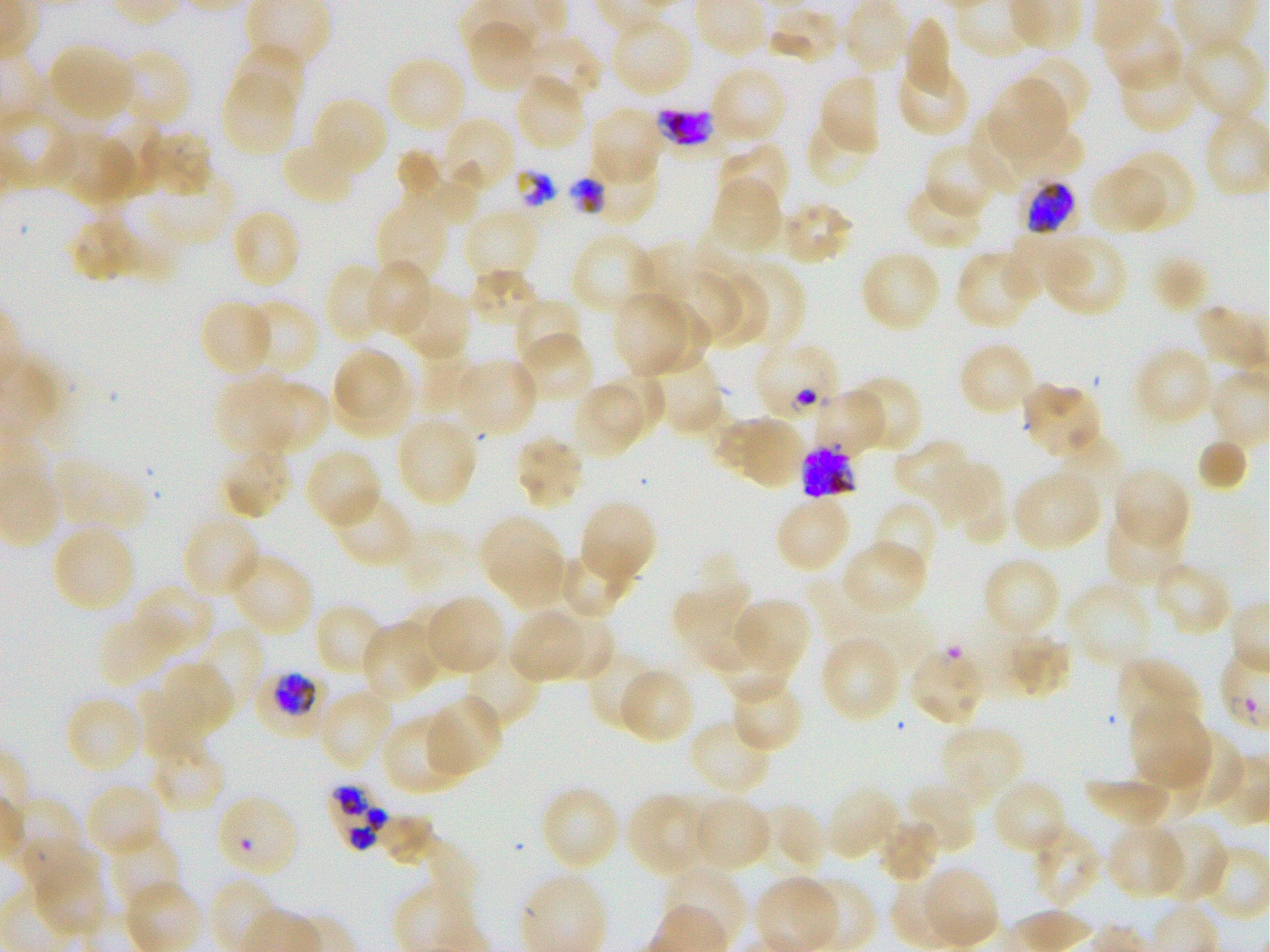

Approximate bounding rectangles given as corner coordinates in pixels from the top-left. Not every red blood cell is marked. A life-cycle stage — or a range of stages, where the recorded stages span more than one — follows each staged infected red blood cell.
Summary:
  - Locations of infected red blood cells: (x1=1025, y1=179, x2=1075, y2=235); (x1=801, y1=443, x2=857, y2=500) late schizont; (x1=250, y1=673, x2=323, y2=738) late trophozoite to early schizont; (x1=325, y1=784, x2=386, y2=852)
  - Locations of red blood cells of indeterminate infection status: (x1=654, y1=98, x2=724, y2=160), (x1=753, y1=340, x2=842, y2=426), (x1=908, y1=645, x2=988, y2=728), (x1=213, y1=792, x2=300, y2=880)
  - Locations of uninfected red blood cells: (x1=840, y1=0, x2=910, y2=76), (x1=766, y1=6, x2=840, y2=65), (x1=465, y1=17, x2=544, y2=93), (x1=903, y1=18, x2=955, y2=99), (x1=1098, y1=18, x2=1185, y2=93), (x1=614, y1=22, x2=687, y2=94), (x1=506, y1=33, x2=602, y2=105), (x1=1179, y1=35, x2=1263, y2=121), (x1=47, y1=42, x2=137, y2=124), (x1=229, y1=43, x2=306, y2=119), (x1=114, y1=47, x2=192, y2=129), (x1=896, y1=52, x2=969, y2=138), (x1=1014, y1=52, x2=1091, y2=133), (x1=1117, y1=56, x2=1201, y2=134), (x1=391, y1=62, x2=465, y2=127), (x1=708, y1=65, x2=788, y2=147), (x1=221, y1=70, x2=300, y2=157), (x1=817, y1=72, x2=881, y2=159), (x1=514, y1=73, x2=587, y2=152), (x1=989, y1=80, x2=1073, y2=163), (x1=308, y1=95, x2=389, y2=181), (x1=588, y1=106, x2=666, y2=186), (x1=95, y1=115, x2=166, y2=195), (x1=968, y1=115, x2=1027, y2=190), (x1=437, y1=116, x2=516, y2=198), (x1=805, y1=116, x2=878, y2=190), (x1=1008, y1=127, x2=1082, y2=182), (x1=139, y1=128, x2=214, y2=198), (x1=51, y1=131, x2=137, y2=203), (x1=281, y1=136, x2=361, y2=207), (x1=716, y1=142, x2=790, y2=220), (x1=923, y1=143, x2=1002, y2=219), (x1=394, y1=149, x2=439, y2=196), (x1=1111, y1=150, x2=1197, y2=232), (x1=573, y1=151, x2=659, y2=227), (x1=413, y1=160, x2=485, y2=218), (x1=146, y1=170, x2=233, y2=242), (x1=1091, y1=170, x2=1163, y2=239), (x1=709, y1=174, x2=785, y2=257), (x1=904, y1=182, x2=987, y2=251), (x1=101, y1=191, x2=186, y2=277), (x1=374, y1=194, x2=451, y2=284), (x1=778, y1=200, x2=854, y2=265), (x1=72, y1=203, x2=135, y2=279), (x1=462, y1=207, x2=542, y2=282), (x1=236, y1=213, x2=300, y2=287), (x1=570, y1=231, x2=654, y2=316), (x1=1005, y1=233, x2=1086, y2=304), (x1=1041, y1=233, x2=1127, y2=317), (x1=859, y1=248, x2=942, y2=334), (x1=955, y1=248, x2=1039, y2=331), (x1=1150, y1=255, x2=1210, y2=313), (x1=365, y1=260, x2=434, y2=339), (x1=723, y1=260, x2=804, y2=354), (x1=324, y1=262, x2=395, y2=344), (x1=467, y1=270, x2=540, y2=330), (x1=707, y1=273, x2=771, y2=348), (x1=677, y1=275, x2=742, y2=340), (x1=397, y1=287, x2=469, y2=359), (x1=613, y1=289, x2=684, y2=374), (x1=512, y1=297, x2=584, y2=373), (x1=198, y1=298, x2=276, y2=377), (x1=249, y1=298, x2=319, y2=375), (x1=648, y1=301, x2=709, y2=373), (x1=516, y1=332, x2=595, y2=406), (x1=958, y1=339, x2=1037, y2=417), (x1=1135, y1=344, x2=1216, y2=427), (x1=334, y1=349, x2=401, y2=419), (x1=419, y1=352, x2=478, y2=415), (x1=454, y1=356, x2=538, y2=439), (x1=641, y1=356, x2=725, y2=436), (x1=593, y1=371, x2=666, y2=433), (x1=842, y1=374, x2=925, y2=454), (x1=333, y1=377, x2=413, y2=434), (x1=219, y1=379, x2=296, y2=458), (x1=1021, y1=381, x2=1096, y2=460), (x1=264, y1=383, x2=329, y2=450), (x1=578, y1=387, x2=643, y2=459), (x1=809, y1=388, x2=889, y2=456), (x1=394, y1=413, x2=479, y2=508), (x1=715, y1=414, x2=808, y2=490), (x1=513, y1=433, x2=586, y2=510), (x1=1196, y1=437, x2=1249, y2=491), (x1=220, y1=442, x2=293, y2=520), (x1=893, y1=442, x2=981, y2=525), (x1=304, y1=447, x2=383, y2=530), (x1=59, y1=453, x2=147, y2=527), (x1=932, y1=458, x2=1008, y2=544), (x1=1111, y1=467, x2=1190, y2=550), (x1=1011, y1=468, x2=1104, y2=553), (x1=330, y1=487, x2=416, y2=568), (x1=774, y1=494, x2=852, y2=575), (x1=577, y1=498, x2=657, y2=588), (x1=872, y1=499, x2=939, y2=581), (x1=1105, y1=512, x2=1185, y2=587), (x1=182, y1=513, x2=262, y2=600), (x1=482, y1=518, x2=557, y2=579), (x1=57, y1=529, x2=134, y2=607), (x1=840, y1=538, x2=928, y2=618), (x1=487, y1=544, x2=583, y2=603), (x1=564, y1=546, x2=639, y2=619), (x1=226, y1=551, x2=315, y2=638), (x1=981, y1=555, x2=1062, y2=640), (x1=1150, y1=561, x2=1233, y2=636), (x1=1066, y1=579, x2=1158, y2=671), (x1=674, y1=582, x2=761, y2=673), (x1=128, y1=586, x2=214, y2=657), (x1=422, y1=594, x2=507, y2=678), (x1=737, y1=597, x2=811, y2=672), (x1=398, y1=602, x2=460, y2=687), (x1=313, y1=603, x2=388, y2=679), (x1=98, y1=609, x2=195, y2=687), (x1=547, y1=609, x2=614, y2=680), (x1=510, y1=611, x2=586, y2=680), (x1=359, y1=620, x2=442, y2=704), (x1=203, y1=630, x2=262, y2=706), (x1=999, y1=632, x2=1072, y2=699), (x1=819, y1=634, x2=902, y2=723), (x1=469, y1=641, x2=539, y2=730), (x1=721, y1=642, x2=789, y2=702), (x1=586, y1=646, x2=658, y2=731), (x1=1116, y1=657, x2=1203, y2=739), (x1=161, y1=662, x2=233, y2=734), (x1=617, y1=667, x2=696, y2=745), (x1=727, y1=674, x2=804, y2=754), (x1=142, y1=687, x2=204, y2=759), (x1=317, y1=687, x2=395, y2=772), (x1=423, y1=694, x2=503, y2=778), (x1=64, y1=695, x2=146, y2=775), (x1=1128, y1=705, x2=1213, y2=794), (x1=383, y1=713, x2=471, y2=794), (x1=688, y1=716, x2=775, y2=796), (x1=937, y1=725, x2=1024, y2=812), (x1=1166, y1=725, x2=1241, y2=807), (x1=149, y1=738, x2=226, y2=813), (x1=1131, y1=756, x2=1203, y2=819), (x1=1088, y1=777, x2=1166, y2=823), (x1=991, y1=779, x2=1068, y2=856), (x1=902, y1=782, x2=978, y2=856), (x1=84, y1=783, x2=165, y2=859), (x1=538, y1=784, x2=621, y2=872), (x1=824, y1=785, x2=902, y2=861), (x1=626, y1=792, x2=715, y2=880), (x1=687, y1=793, x2=773, y2=872), (x1=11, y1=797, x2=81, y2=870), (x1=760, y1=803, x2=829, y2=877), (x1=383, y1=811, x2=441, y2=866), (x1=1148, y1=818, x2=1228, y2=904), (x1=879, y1=819, x2=938, y2=882), (x1=1029, y1=821, x2=1102, y2=910), (x1=1107, y1=821, x2=1188, y2=900), (x1=117, y1=834, x2=181, y2=905), (x1=25, y1=835, x2=96, y2=890), (x1=1183, y1=837, x2=1268, y2=921), (x1=431, y1=843, x2=477, y2=905), (x1=663, y1=864, x2=748, y2=945), (x1=917, y1=865, x2=999, y2=948), (x1=40, y1=868, x2=107, y2=940), (x1=803, y1=878, x2=878, y2=952)
  - Preparation: thin blood smear
  - Field of view: one from this slide
  - Stain: Giemsa
  - Donor blood group: O+
  - Objective: 100x, oil immersion, numerical aperture 1.25
  - Image size: 1270×952 pixels
  - Culture: P. falciparum strain 3D7, static, in vitro